Assess this cell for malaria.
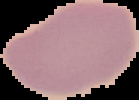
Uninfected.

From a thin blood film. Segmented cell region on a black background. Image is 139×100 pixels.